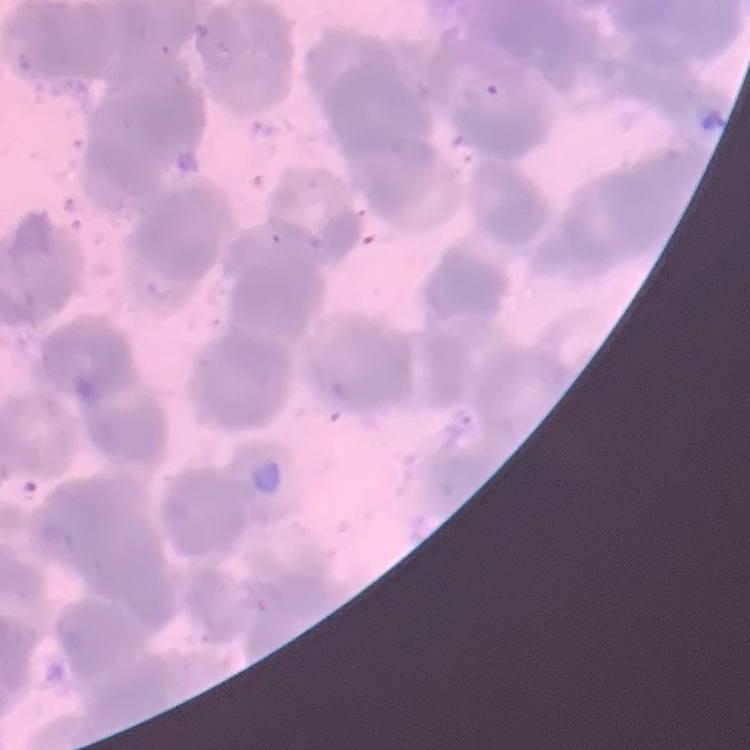 The erythrocytes show rouleaux formation. One tile cut from a larger photomicrograph. Thin blood film. Field's or Giemsa stain.